Locate every blood parasite and identify its species.
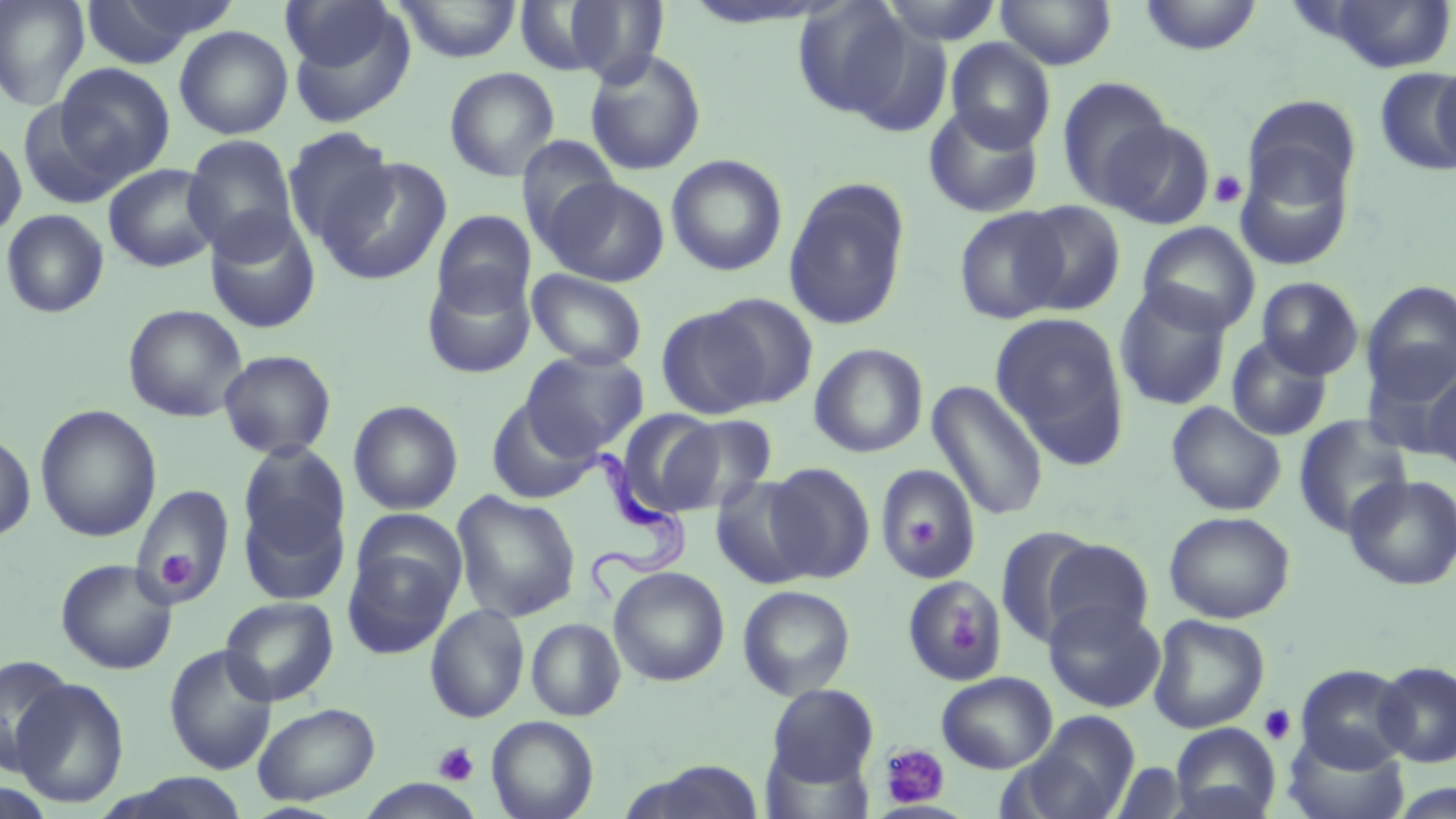
Approximate bounding boxes as (x1,y1)-(x2,y2) corner pairs in pixels.
Trypanosoma brucei: (577,446)-(684,599).
No Plasmodium falciparum, Plasmodium ovale, Plasmodium malariae, Plasmodium vivax, or Babesia divergens observed.

Summary:
  - Platelet locations: (1208,169)-(1248,209), (908,517)-(935,546), (159,551)-(193,591), (946,605)-(986,656), (1258,704)-(1297,746), (433,742)-(479,787), (878,744)-(951,809)
  - Uninfected red blood cell locations: (0,0)-(90,110), (79,0)-(234,69), (280,0)-(402,78), (395,0)-(522,63), (879,0)-(1004,45), (995,0)-(1117,70), (1137,0)-(1264,56), (1321,0)-(1456,73), (549,1)-(671,84), (791,1)-(916,121), (174,25)-(293,139), (945,38)-(1056,152), (583,48)-(708,177), (1431,59)-(1456,173), (53,63)-(175,184), (444,67)-(561,182), (1374,67)-(1456,177), (1056,77)-(1172,210), (1243,95)-(1361,208), (18,100)-(130,209), (922,104)-(1046,219), (1100,117)-(1217,230), (281,126)-(397,247), (0,133)-(27,241), (182,134)-(300,260), (516,135)-(621,249), (1232,147)-(1356,272), (666,154)-(788,276), (319,156)-(451,286), (103,163)-(221,272), (542,177)-(670,287), (784,179)-(911,331), (1016,200)-(1127,316), (954,207)-(1070,324), (1,209)-(109,318), (431,210)-(535,316), (204,212)-(322,334), (1137,222)-(1261,335), (421,267)-(537,379), (527,269)-(648,371), (1256,276)-(1364,380), (1362,280)-(1456,395), (1114,284)-(1233,411), (706,293)-(819,408), (122,303)-(248,422), (655,306)-(770,419), (990,312)-(1131,467), (1226,335)-(1333,441), (809,342)-(928,458), (218,349)-(337,459), (521,349)-(648,458), (1363,349)-(1456,461), (1424,369)-(1456,473), (927,379)-(1049,521), (486,398)-(600,505), (348,400)-(463,515), (1166,401)-(1287,516), (35,405)-(162,542), (616,409)-(724,516), (667,413)-(780,514), (1293,415)-(1414,538), (0,432)-(36,543), (237,442)-(351,559), (765,462)-(876,583), (876,463)-(982,583), (1344,474)-(1456,590), (710,475)-(818,589), (130,484)-(235,607), (451,490)-(581,623), (238,496)-(350,605), (350,508)-(468,611), (1164,510)-(1295,624), (995,526)-(1102,647), (1041,538)-(1155,645), (342,547)-(458,660), (55,558)-(177,675), (608,566)-(729,687), (900,576)-(1006,686), (737,585)-(856,700), (220,596)-(338,706), (1044,599)-(1165,712), (425,603)-(530,723), (1148,614)-(1270,734), (525,618)-(625,721), (164,645)-(278,775), (1,655)-(75,773), (1372,661)-(1456,767), (1295,664)-(1414,772), (937,671)-(1058,773), (9,676)-(130,808), (767,684)-(879,787), (252,702)-(380,805), (1011,711)-(1140,819), (486,715)-(599,819), (1169,723)-(1280,819), (1284,731)-(1409,819), (625,759)-(766,819), (1111,762)-(1189,818), (106,773)-(252,818), (1386,783)-(1455,819)
  - Slide-level diagnosis: Trypanosoma brucei
  - Modality: light microscopy
  - Magnification: 1000x
  - Field of view: one of a larger specimen
  - Stain: May-Grünwald-Giemsa
  - Image size: 1456×819 pixels
  - Preparation: thin blood smear